Assess for parasitized red blood cells.
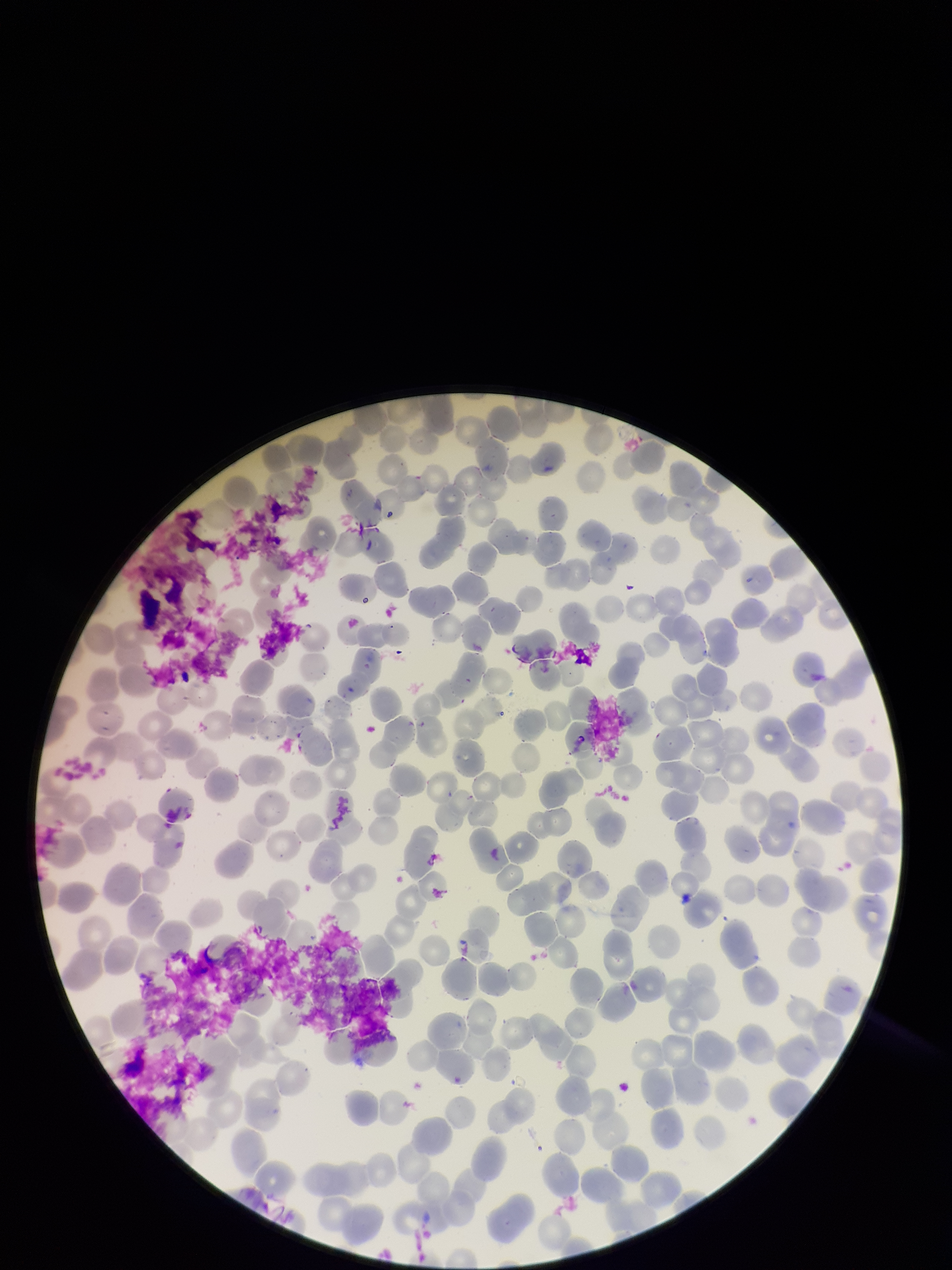
None detected.

red blood cell count = 251
image size = 952×1270 pixels
preparation = thin
parasitized red blood cell count = 0
field of view = single
stain = Giemsa
capture = smartphone photograph through the microscope eyepiece
patient malaria status = negative